State which cell type is depicted.
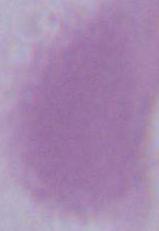
This is an erythrocyte.

magnification: 1000x
modality: photomicrograph